Identify the parasite.
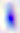

Toxoplasma gondii.

modality = micrograph
magnification = 400x